Outline each uninfected red blood cell.
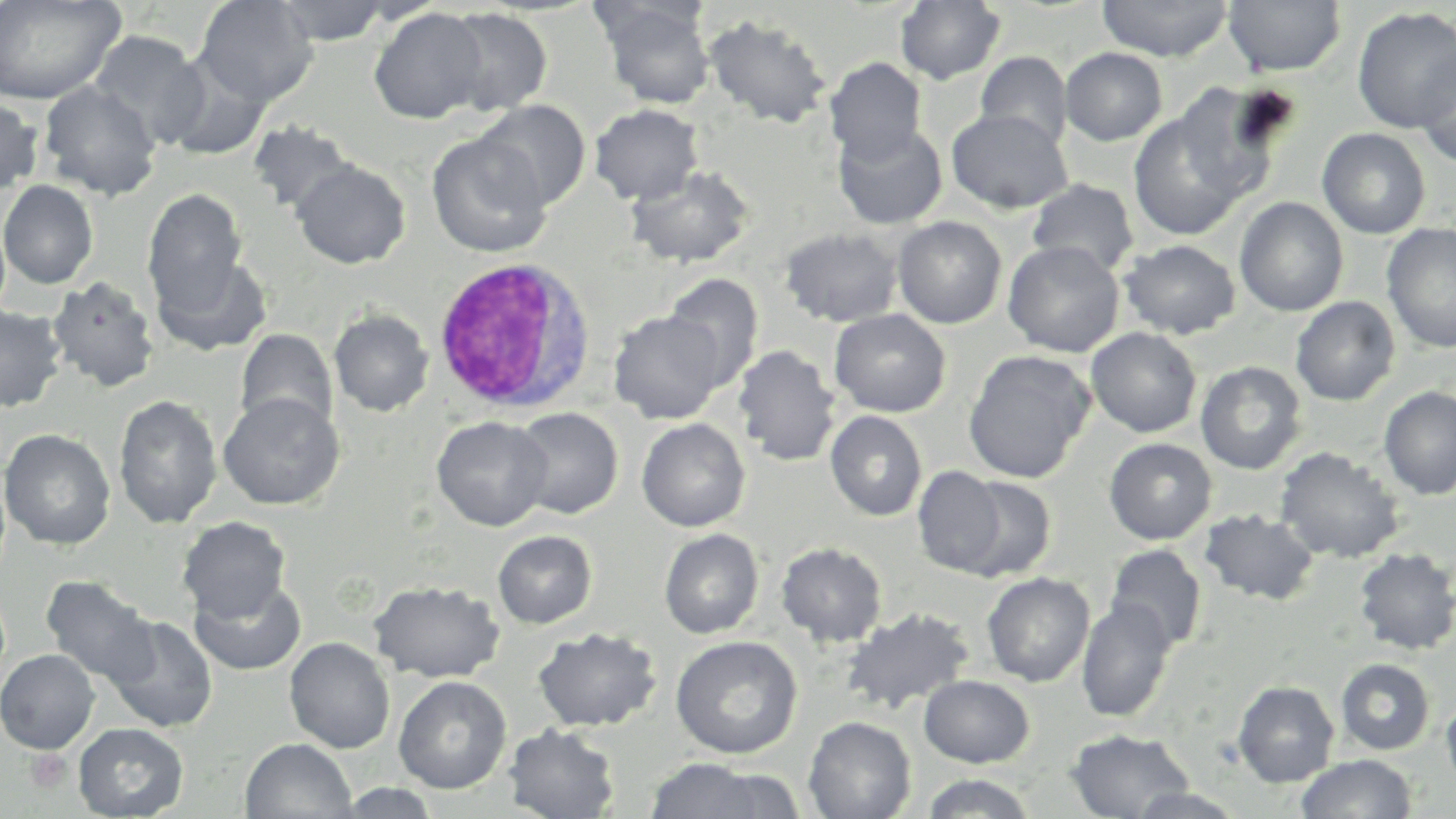

Approximate bounding boxes as (x1,y1)-(x2,y2) corner pairs in pixels.
Uninfected red blood cells: (0,0)-(126,105), (195,0)-(317,108), (273,0)-(394,46), (1097,0)-(1233,62), (1222,0)-(1346,77), (895,1)-(1006,85), (597,2)-(716,109), (1352,6)-(1455,134), (368,7)-(488,124), (441,7)-(553,116), (703,14)-(832,130), (87,30)-(208,147), (1060,47)-(1167,146), (1414,50)-(1455,168), (976,51)-(1073,151), (161,52)-(271,161), (824,57)-(927,165), (39,81)-(162,200), (1173,83)-(1288,205), (0,98)-(42,197), (477,100)-(590,209), (589,104)-(704,205), (946,108)-(1073,214), (1128,109)-(1248,241), (247,120)-(356,216), (832,121)-(948,230), (1316,127)-(1431,239), (427,133)-(553,258), (290,160)-(411,269), (625,165)-(755,270), (1027,179)-(1140,278), (0,180)-(99,289), (143,187)-(249,314), (1234,197)-(1348,316), (893,216)-(1007,329), (1381,223)-(1456,354), (780,227)-(903,327), (1120,239)-(1241,340), (1003,240)-(1124,358), (150,252)-(273,358), (663,272)-(764,391), (48,275)-(160,393), (1291,296)-(1400,406), (0,305)-(67,413), (329,309)-(434,417), (608,309)-(728,424), (829,309)-(951,417), (1085,327)-(1202,438), (234,329)-(338,437), (732,345)-(842,467), (963,349)-(1096,484), (1195,361)-(1307,475), (1379,386)-(1456,500), (218,392)-(344,509), (113,394)-(223,530), (511,407)-(623,519), (825,410)-(927,522), (431,416)-(553,531), (636,418)-(751,532), (0,428)-(116,551), (1104,438)-(1217,545), (1275,446)-(1405,563), (912,465)-(1007,577), (957,475)-(1058,582), (1199,508)-(1320,606), (177,516)-(291,622), (659,528)-(764,639), (493,530)-(597,629), (776,542)-(888,647), (1104,544)-(1207,652), (1353,547)-(1456,656), (982,572)-(1095,687), (41,575)-(157,687), (189,577)-(307,676), (369,579)-(505,684), (1076,599)-(1177,723), (840,607)-(975,715), (103,614)-(219,734), (533,627)-(662,732), (670,635)-(803,759), (284,637)-(395,754), (0,649)-(100,754), (1336,658)-(1435,755), (919,675)-(1035,768), (393,676)-(512,794), (1232,680)-(1339,787), (1441,697)-(1456,791), (803,716)-(917,819), (72,723)-(189,818), (503,723)-(621,818), (1066,728)-(1194,818), (240,737)-(357,818), (1295,754)-(1418,819), (642,758)-(783,818), (698,768)-(805,817), (918,773)-(1039,818), (334,784)-(443,818), (1126,787)-(1249,818).

slide_level_diagnosis: negative for blood parasites
field_of_view: one of a larger specimen
platelet_locations: 'approximate bounding boxes as (x1,y1)-(x2,y2) corner pairs in pixels: (25,749)-(72,794)'
magnification: 1000x
image_size: 1456×819 pixels
stain: May-Grünwald-Giemsa
white_blood_cell_locations: 'approximate bounding boxes as (x1,y1)-(x2,y2) corner pairs in pixels: (430,256)-(597,415)'
modality: light microscopy
preparation: thin blood film